Locate and identify every blood parasite.
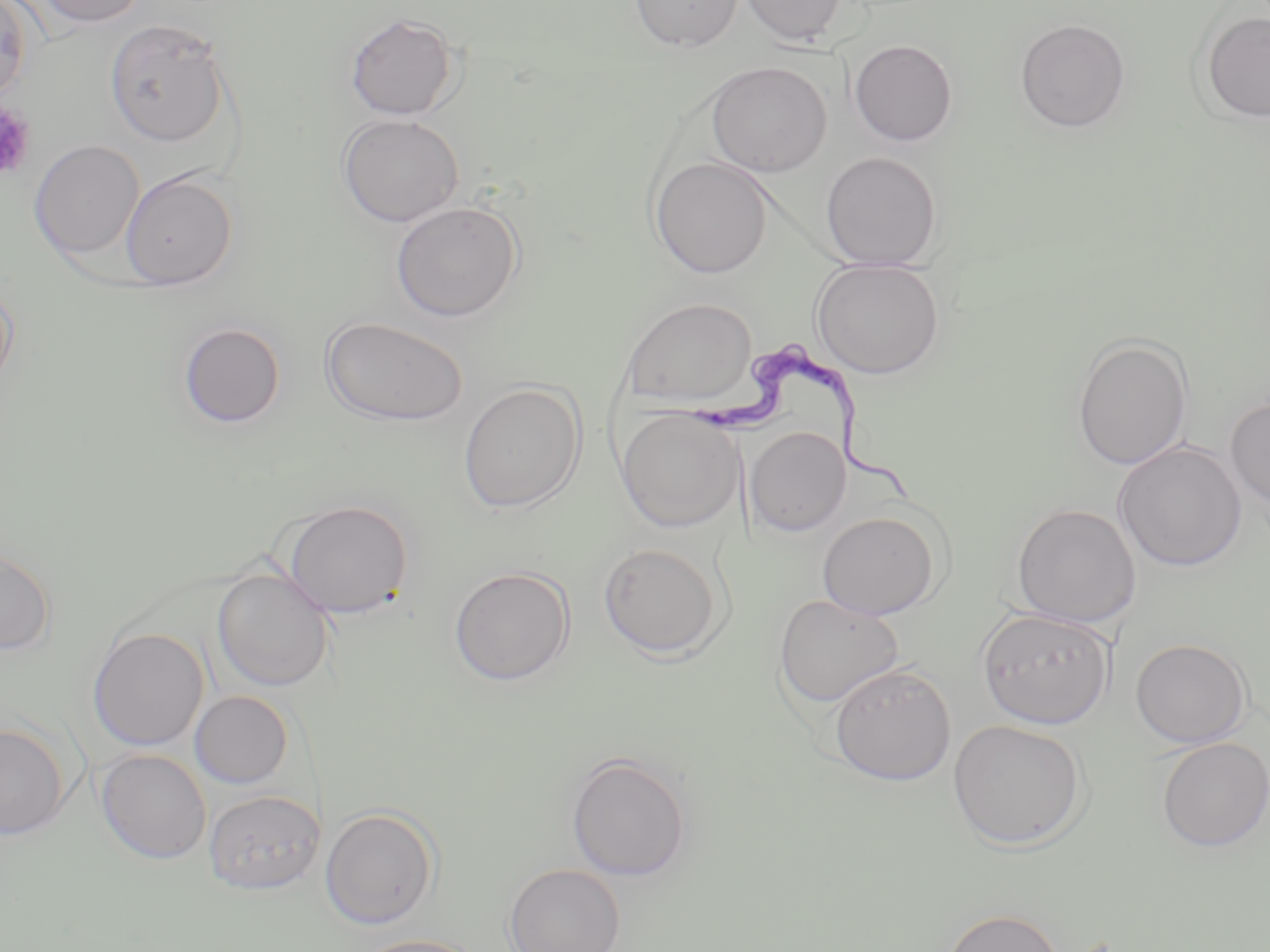
Approximate bounding boxes as [x1, y1, x2, y2] in pixels.
Trypanosoma brucei: [693, 345, 919, 505].
No Plasmodium falciparum, Plasmodium ovale, Plasmodium malariae, Plasmodium vivax, or Babesia divergens observed.

Platelet locations: [0, 102, 35, 180]. Uninfected red blood cell locations: [0, 0, 34, 103], [31, 0, 147, 28], [628, 0, 744, 52], [737, 0, 850, 47], [1198, 10, 1270, 123], [344, 12, 460, 120], [104, 18, 231, 147], [1014, 18, 1132, 133], [849, 39, 958, 146], [706, 60, 832, 176], [337, 114, 464, 227], [29, 140, 144, 260], [820, 151, 943, 269], [650, 156, 774, 278], [120, 170, 239, 290], [390, 200, 524, 323], [810, 258, 946, 379], [0, 275, 19, 396], [621, 296, 758, 408], [320, 314, 469, 427], [177, 321, 286, 429], [1070, 333, 1193, 470], [457, 381, 587, 514], [1225, 395, 1270, 513], [616, 409, 743, 532], [745, 426, 851, 537], [1113, 440, 1247, 572], [279, 498, 415, 620], [1010, 503, 1142, 627], [817, 510, 942, 620], [598, 541, 725, 660], [0, 545, 56, 655], [448, 565, 575, 686], [212, 569, 334, 692], [773, 593, 904, 710], [965, 602, 1102, 848], [976, 608, 1115, 729], [87, 627, 209, 751], [1130, 637, 1252, 748], [830, 663, 956, 786], [190, 691, 293, 789], [947, 719, 1088, 850], [0, 722, 71, 841], [1155, 737, 1270, 852], [96, 748, 212, 866], [565, 751, 694, 881], [204, 789, 323, 895], [319, 806, 441, 930], [504, 863, 626, 952], [942, 907, 1065, 952], [351, 934, 485, 952]. Slide-level diagnosis: Trypanosoma brucei. Optical microscopy. 1000x magnification. May-Grünwald-Giemsa stain. Image is 1270×952 pixels. Thin blood smear. One field of a larger specimen.